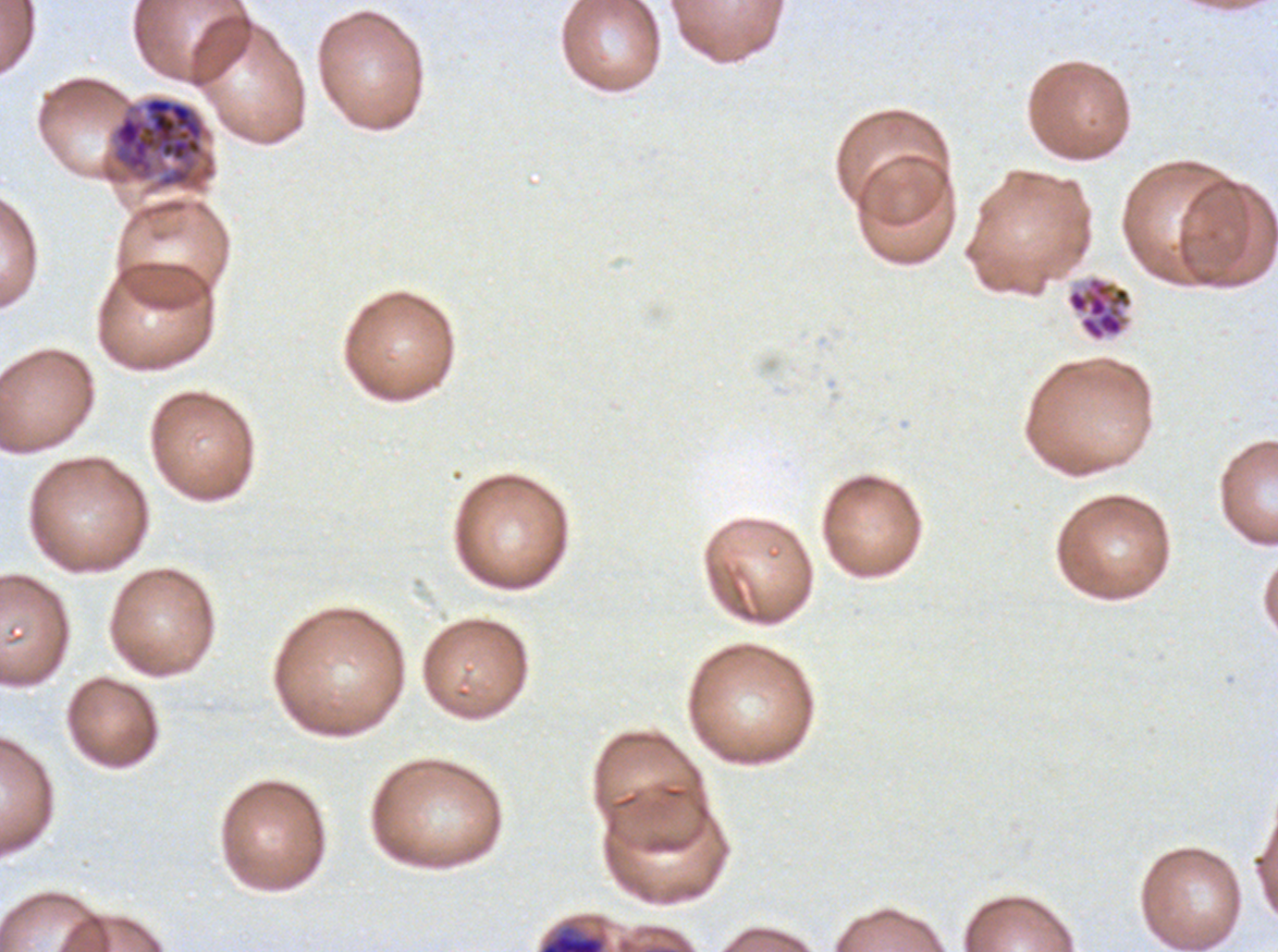

Approximate bounding rectangles given as corner coordinates in pixels from the top-left.
Summary:
  - Segmenter locations: (x1=1066, y1=276, x2=1133, y2=341)
  - Debris locations: (x1=538, y1=923, x2=608, y2=951)
  - Late schizont locations: (x1=113, y1=95, x2=205, y2=188)
  - Image size: 1278×952 pixels
  - Life-cycle stages observed: late schizont, segmenter
  - Specimen: ex-vivo Plasmodium falciparum culture from a patient in The Gambia, grown for 24 to 48 hours
  - Field of view: sub-image separated from a larger composite
  - Stain: Giemsa
  - Preparation: thin blood smear